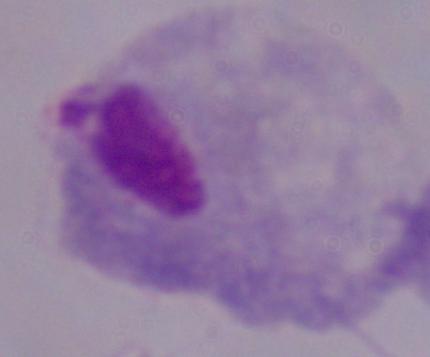
{
  "modality": "micrograph",
  "magnification": "1000x",
  "identification": "trichomonad"
}